Name the blood parasite species.
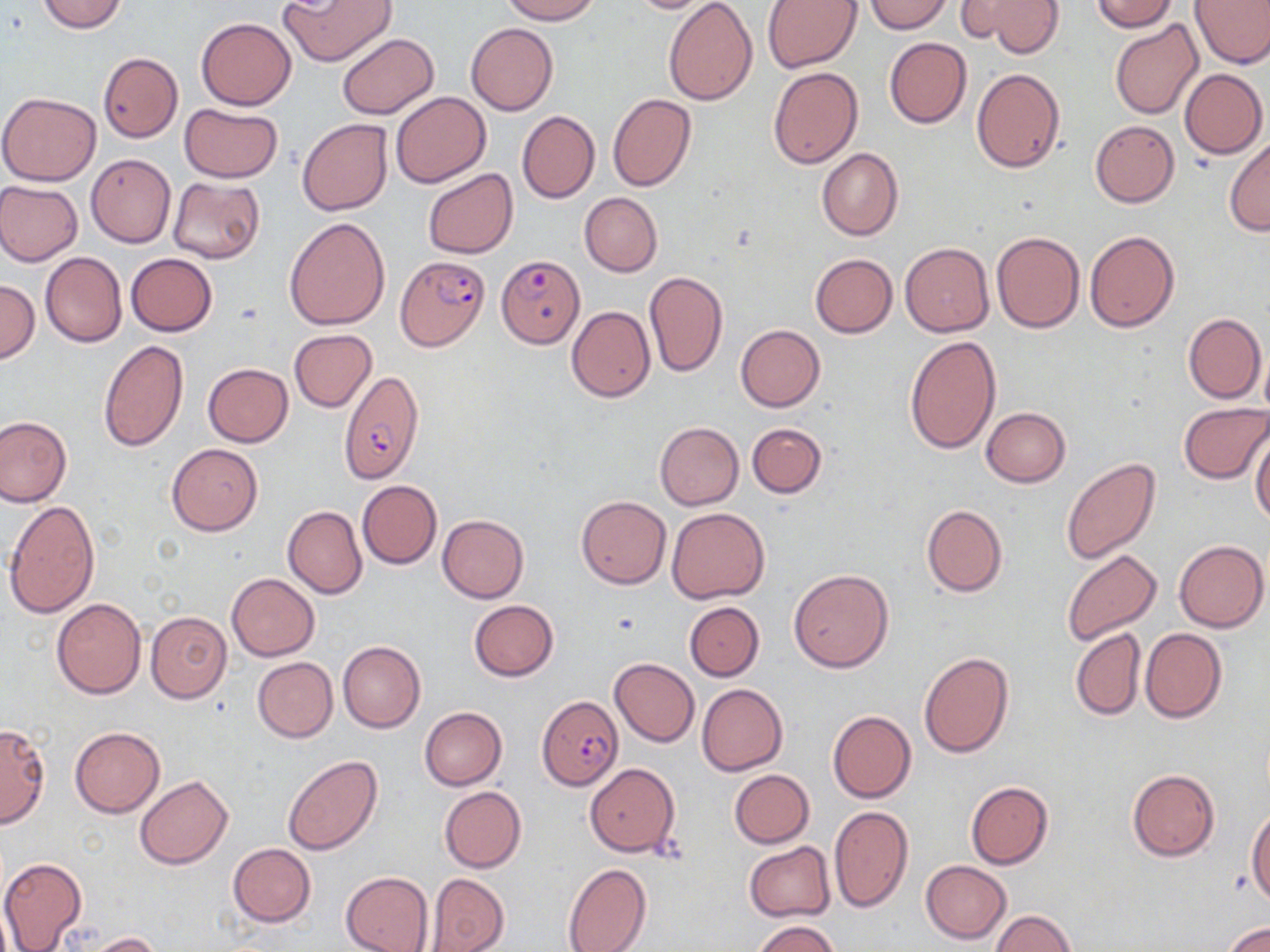

Plasmodium falciparum.

Summary:
  - Coordinate format: approximate bounding boxes as (x1, y1, x2, y2) in pixels
  - Uninfected red blood cell locations: (36, 0, 128, 33), (279, 0, 396, 66), (498, 0, 603, 24), (625, 0, 725, 14), (663, 0, 757, 104), (862, 0, 954, 33), (1086, 0, 1179, 32), (1189, 0, 1270, 69), (763, 1, 863, 73), (966, 1, 1065, 56), (196, 18, 296, 110), (1109, 19, 1204, 120), (466, 22, 558, 116), (337, 34, 439, 118), (883, 38, 972, 128), (98, 52, 183, 142), (768, 67, 862, 168), (972, 68, 1067, 174), (1179, 68, 1267, 158), (0, 91, 103, 186), (390, 91, 491, 188), (607, 93, 696, 193), (179, 103, 282, 182), (517, 110, 600, 203), (297, 118, 392, 216), (1090, 120, 1180, 207), (1224, 135, 1269, 237), (817, 147, 902, 241), (86, 154, 176, 247), (422, 168, 518, 258), (167, 176, 264, 262), (0, 181, 82, 265), (579, 192, 663, 276), (284, 218, 390, 330), (1084, 230, 1180, 333), (992, 231, 1085, 333), (900, 243, 995, 337), (40, 251, 127, 348), (126, 253, 217, 336), (809, 254, 898, 338), (644, 271, 728, 377), (0, 280, 40, 363), (567, 305, 655, 401), (1182, 312, 1266, 404), (735, 324, 825, 412), (289, 329, 376, 412), (904, 335, 1001, 454), (98, 339, 189, 454), (202, 363, 294, 447), (1179, 403, 1270, 484), (981, 407, 1071, 488), (0, 415, 72, 508), (655, 422, 744, 510), (747, 422, 825, 498), (1251, 430, 1270, 526), (167, 444, 264, 535), (1059, 459, 1160, 565), (357, 480, 442, 569), (576, 496, 671, 589), (5, 501, 100, 619), (921, 504, 1007, 598), (283, 506, 367, 599), (666, 507, 770, 603), (437, 514, 528, 603), (1174, 540, 1268, 632), (1061, 549, 1162, 647), (789, 569, 894, 672), (227, 574, 319, 660), (51, 597, 146, 698), (468, 599, 558, 681), (685, 601, 765, 680), (146, 611, 232, 703), (1070, 626, 1147, 721), (1139, 628, 1226, 723), (338, 641, 425, 732), (919, 651, 1013, 758), (252, 657, 337, 741), (610, 657, 699, 747), (696, 684, 788, 775), (419, 707, 507, 790), (827, 710, 916, 803), (0, 722, 50, 828), (69, 726, 165, 818), (282, 754, 383, 856), (585, 763, 679, 857), (729, 769, 814, 848), (1127, 769, 1220, 861), (134, 775, 233, 868), (965, 781, 1054, 868), (439, 785, 526, 874), (828, 806, 913, 912), (1247, 807, 1269, 905), (743, 842, 836, 921), (228, 843, 317, 927), (0, 855, 87, 952), (921, 860, 1011, 944), (562, 863, 651, 952), (341, 872, 434, 952), (426, 873, 507, 951), (991, 910, 1075, 952), (750, 919, 840, 952), (1224, 921, 1270, 952), (81, 931, 163, 951)
  - Plasmodium falciparum-infected red blood cell locations: (395, 254, 488, 352), (496, 255, 585, 348), (337, 371, 424, 484), (538, 695, 621, 792)
  - Preparation: thin blood smear
  - Field of view: single
  - Stain: May-Grünwald-Giemsa
  - Magnification: 1000x
  - Image size: 1270×952 pixels
  - Modality: light microscopy